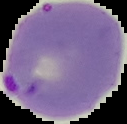

image type = cell region segmented out of the field of view; surrounding area masked to black
malaria status = parasitized
preparation = thin blood smear
image size = 127×124 pixels